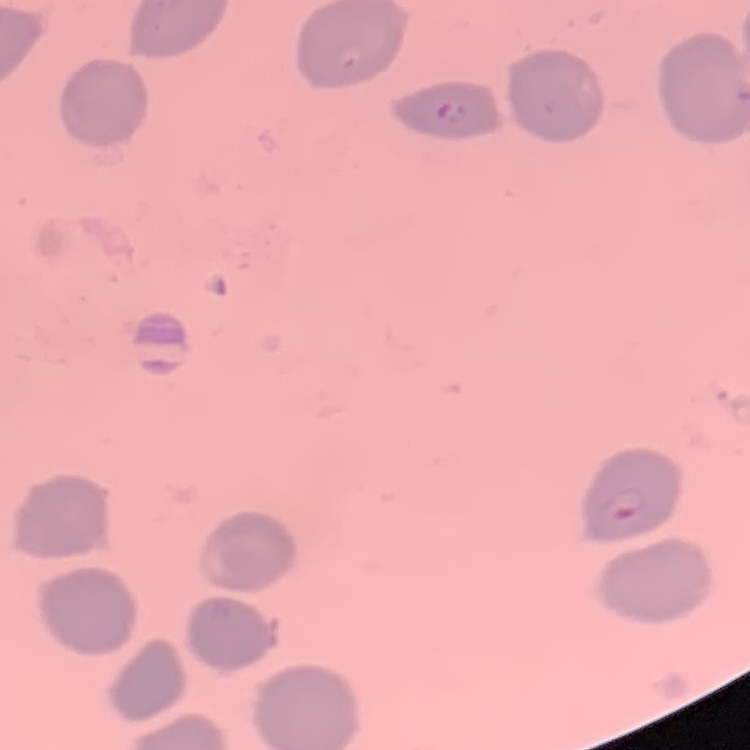

erythrocyte_morphology: no rouleaux formation
preparation: thin peripheral smear
stain: Field's or Giemsa
image_type: square crop of a larger photomicrograph